State which parasite is depicted.
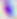

This is Toxoplasma gondii.

magnification = 400x
modality = micrograph